Give a bounding box for every leukocyte visible.
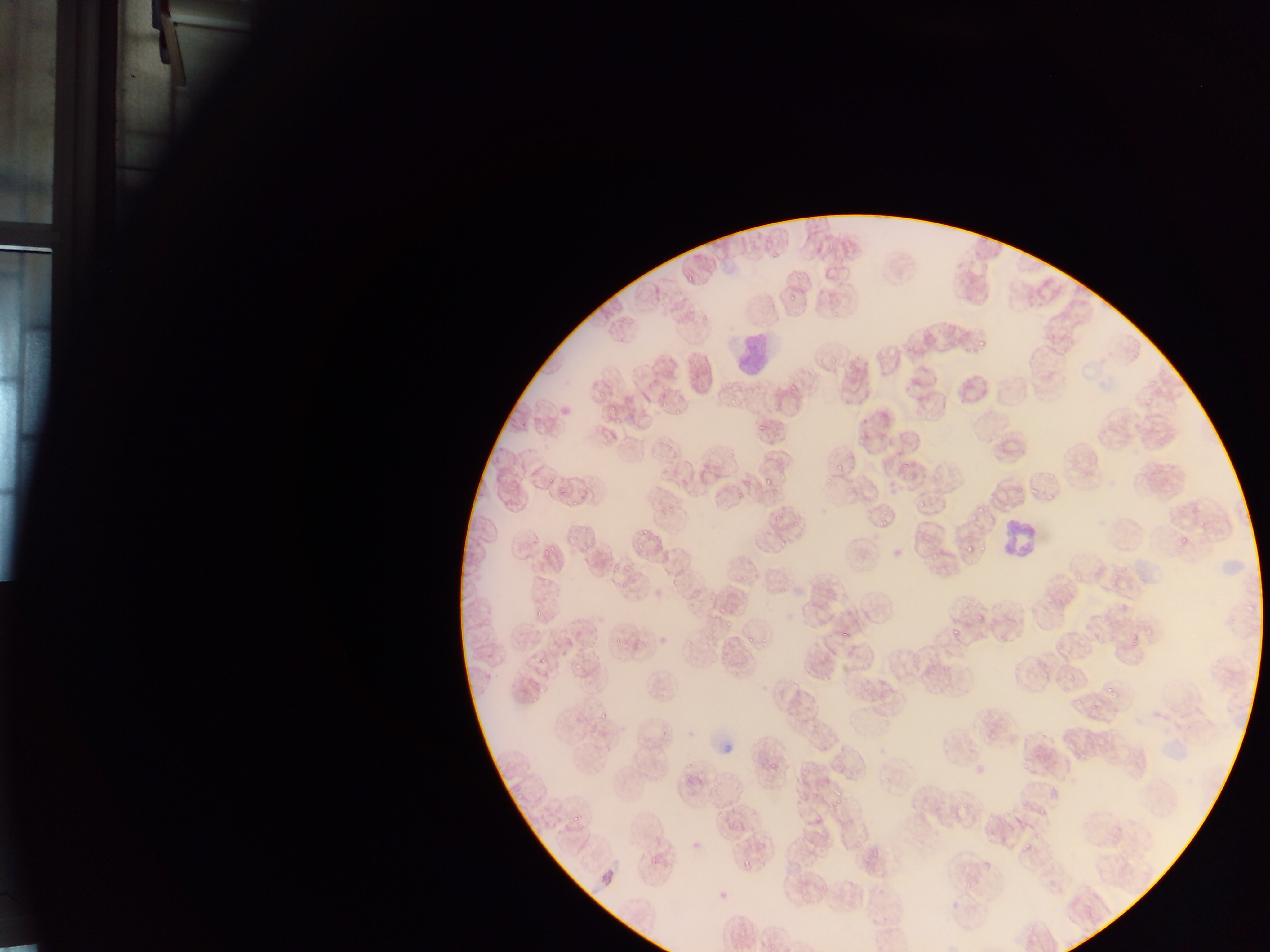
Approximate bounding boxes as [left, top, right, bottom] in pixels.
Leukocytes: [738, 331, 774, 383], [992, 516, 1041, 562].

Summary:
  - Malaria parasite locations: [972, 340, 987, 354], [783, 380, 797, 396], [660, 400, 670, 406], [672, 406, 684, 420], [753, 423, 768, 432], [834, 457, 848, 471], [821, 470, 839, 485], [759, 473, 777, 488], [1025, 482, 1038, 497], [1047, 490, 1054, 506], [914, 495, 930, 508], [975, 502, 986, 514], [770, 506, 788, 524], [877, 518, 888, 529], [532, 526, 547, 547], [640, 530, 652, 540], [1173, 530, 1192, 550], [541, 541, 562, 557], [963, 541, 981, 554], [773, 542, 789, 551], [634, 546, 647, 552], [929, 546, 941, 562], [670, 576, 681, 583], [717, 607, 730, 617], [531, 609, 547, 618], [974, 617, 988, 626], [719, 618, 729, 632], [948, 627, 958, 639], [743, 632, 757, 645], [631, 638, 645, 652], [1033, 665, 1053, 679], [1064, 670, 1082, 686], [1107, 686, 1117, 700], [1087, 695, 1103, 711], [596, 711, 608, 720], [657, 726, 670, 740], [767, 760, 781, 774], [682, 761, 700, 784], [832, 782, 846, 802], [513, 792, 524, 807], [568, 814, 582, 827], [864, 840, 890, 862], [741, 858, 757, 871]
  - Field of view: single
  - Preparation: thin blood film
  - Image size: 1270×952 pixels
  - Capture: mobile-phone photograph through a microscope
  - Country: Ghana